Assess for malaria.
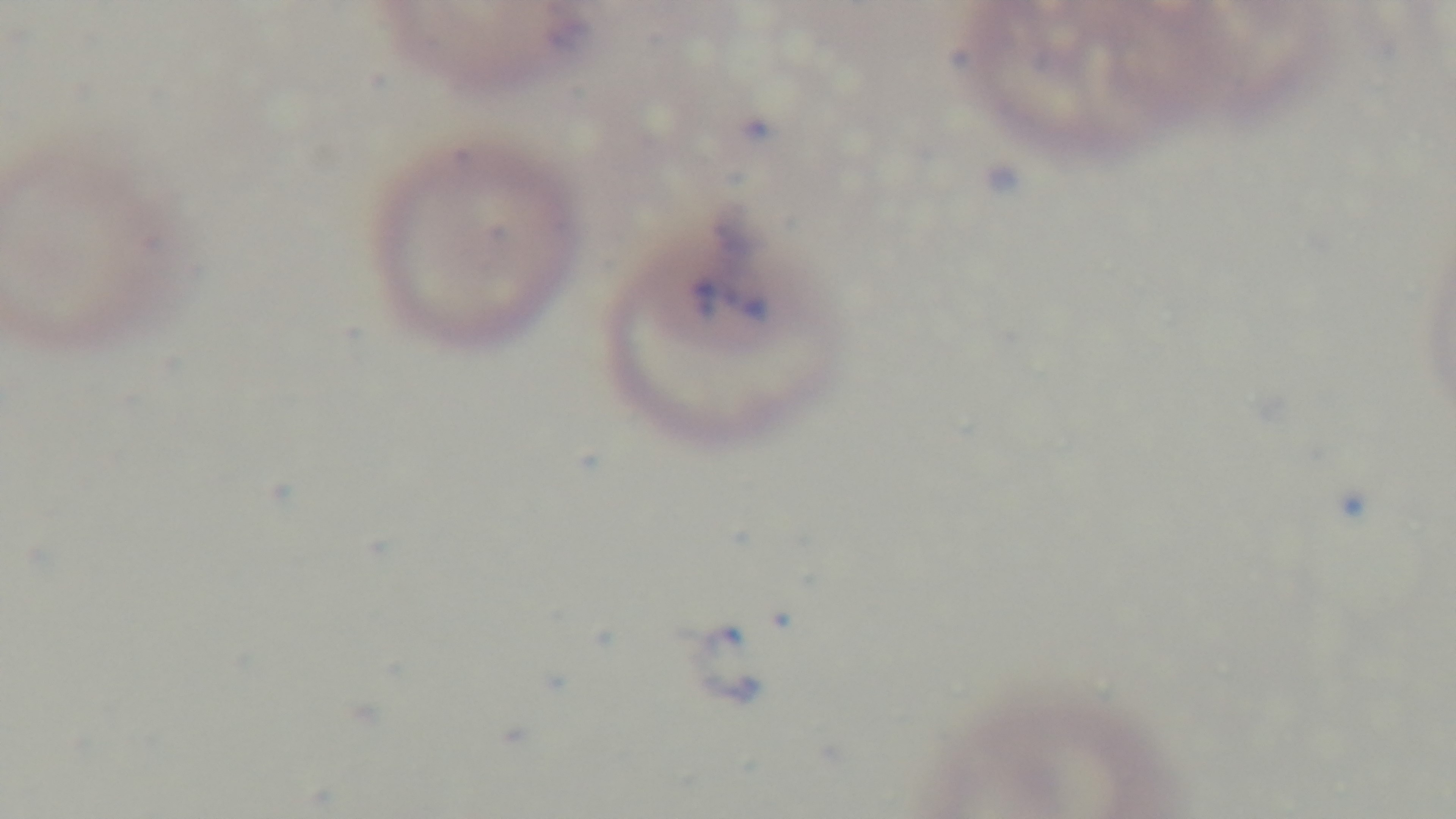

Positive.

capture: mounted 4K digital camera
modality: light microscopy
preparation: thin blood film
objective: 100x oil immersion
stain: Giemsa
field_of_view: one from the slide